Name the cell type shown.
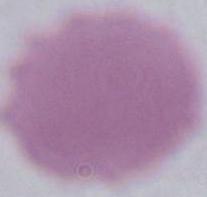
An erythrocyte.

magnification = 1000x
modality = micrograph